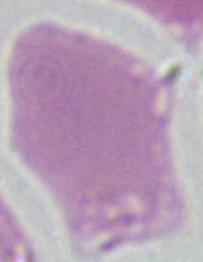 Captured at 1000x magnification. An erythrocyte is shown. Micrograph.